Assess for Plasmodium parasites.
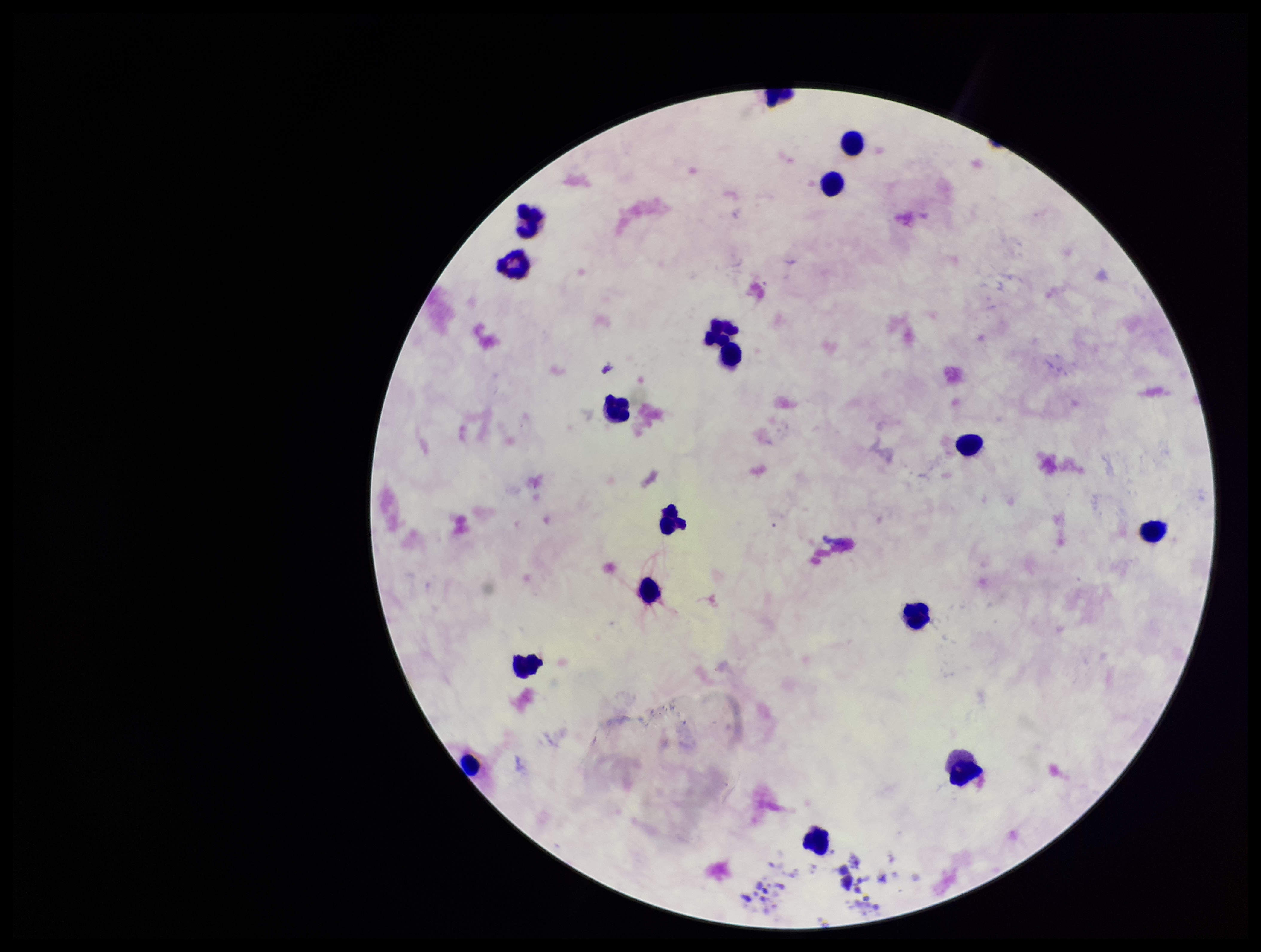

None detected.

Summary:
  - Stain: Giemsa
  - Capture: smartphone photograph through the microscope eyepiece
  - Image size: 1261×952 pixels
  - Preparation: thick
  - Leukocyte count: 15
  - Field of view: single
  - Patient malaria status: negative
  - Parasite count: 0